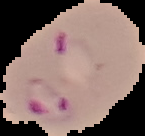

Summary:
  - Image type: segmented cell region on a black background
  - Preparation: thin blood smear
  - Image size: 145×136 pixels
  - Malaria status: parasitized